Locate every blood parasite and identify its species.
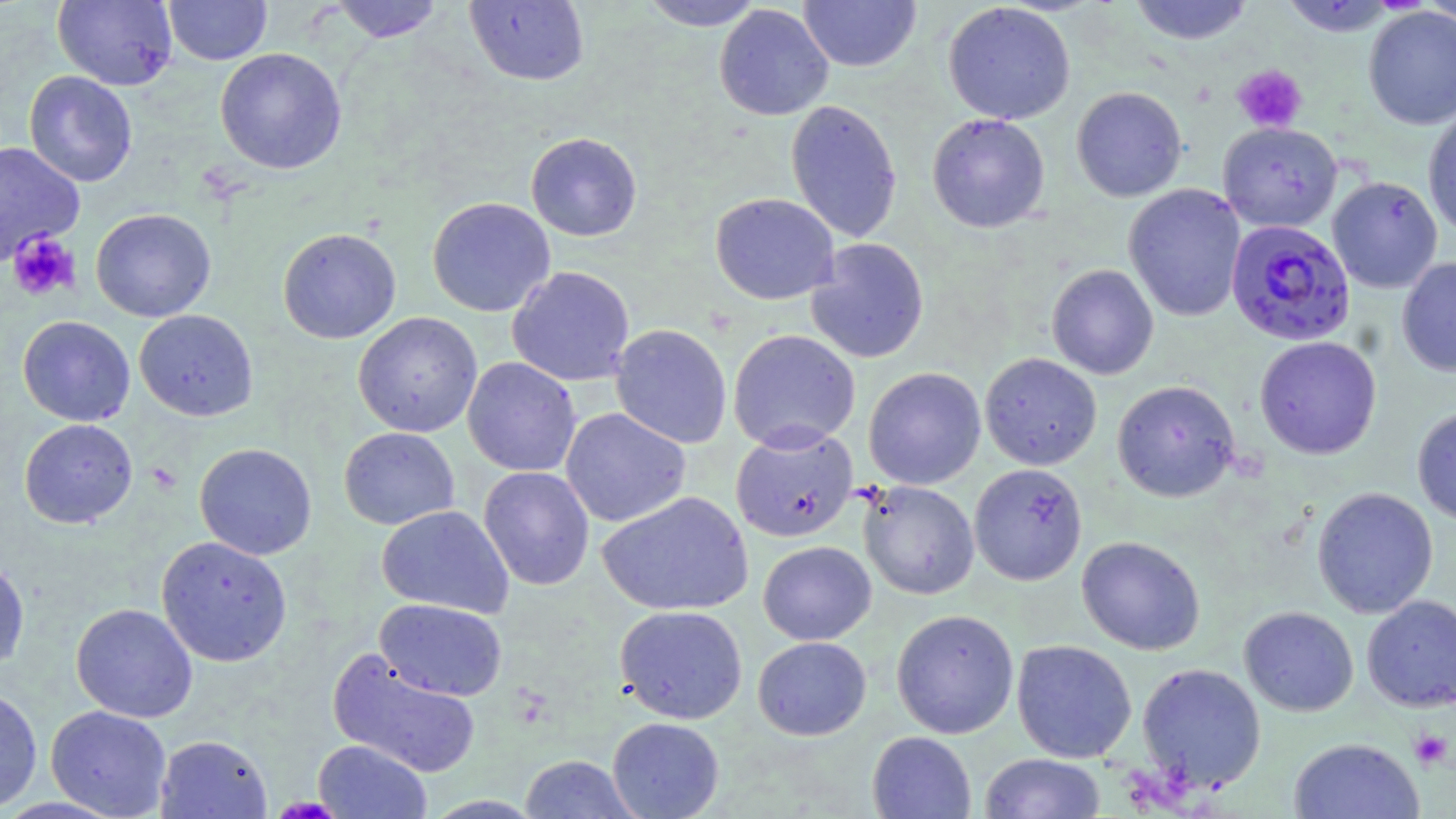
Approximate bounding boxes as (x1,y1)-(x2,y2) corner pairs in pixels.
Plasmodium falciparum-infected red blood cells: (1225,218)-(1356,346).
No Plasmodium ovale, Plasmodium malariae, Plasmodium vivax, Babesia divergens, or Trypanosoma brucei observed.

Platelet locations: (1232,64)-(1307,133), (7,231)-(81,301), (147,462)-(182,495), (1409,729)-(1452,770). Uninfected red blood cell locations: (52,0)-(178,90), (163,0)-(272,65), (464,0)-(589,87), (637,0)-(766,31), (798,0)-(922,72), (1128,0)-(1255,45), (328,1)-(446,43), (1279,1)-(1400,36), (1418,1)-(1456,30), (942,2)-(1076,125), (714,4)-(834,121), (1363,6)-(1456,131), (215,47)-(347,175), (23,71)-(138,187), (1071,86)-(1187,202), (785,99)-(902,243), (1422,105)-(1456,240), (926,113)-(1051,233), (1218,121)-(1343,232), (526,132)-(642,241), (0,141)-(85,265), (1327,175)-(1443,293), (1123,183)-(1246,322), (710,192)-(840,305), (427,197)-(555,317), (91,208)-(216,322), (277,227)-(401,344), (806,238)-(929,363), (1397,256)-(1456,377), (1046,264)-(1159,380), (507,265)-(635,387), (134,309)-(258,421), (353,312)-(482,437), (17,316)-(135,426), (610,324)-(732,449), (728,329)-(861,452), (1254,336)-(1382,459), (980,353)-(1102,470), (462,357)-(581,477), (863,367)-(986,489), (1112,380)-(1240,502), (1412,406)-(1456,526), (560,407)-(691,527), (19,418)-(138,528), (730,426)-(858,543), (338,427)-(459,530), (194,443)-(317,560), (969,462)-(1087,585), (478,466)-(595,591), (859,480)-(979,599), (1312,487)-(1438,618), (597,491)-(754,616), (376,505)-(513,618), (155,536)-(292,666), (1077,536)-(1205,655), (758,541)-(876,645), (0,555)-(30,675), (1362,594)-(1456,712), (375,598)-(507,701), (71,603)-(198,722), (615,605)-(748,724), (1239,606)-(1358,716), (891,609)-(1019,738), (753,636)-(871,740), (1011,639)-(1138,762), (327,648)-(481,779), (1136,662)-(1267,792), (0,685)-(42,813), (46,705)-(172,818), (607,717)-(724,819), (867,731)-(977,819), (155,734)-(273,819), (1288,738)-(1425,819), (312,739)-(432,819), (979,753)-(1106,818), (519,754)-(639,818), (420,795)-(546,818). Slide-level diagnosis: Plasmodium falciparum. Light microscopy. May-Grünwald-Giemsa stain. Thin blood film. Image is 1456×819 pixels. One field of a larger specimen. Captured at 1000x magnification.